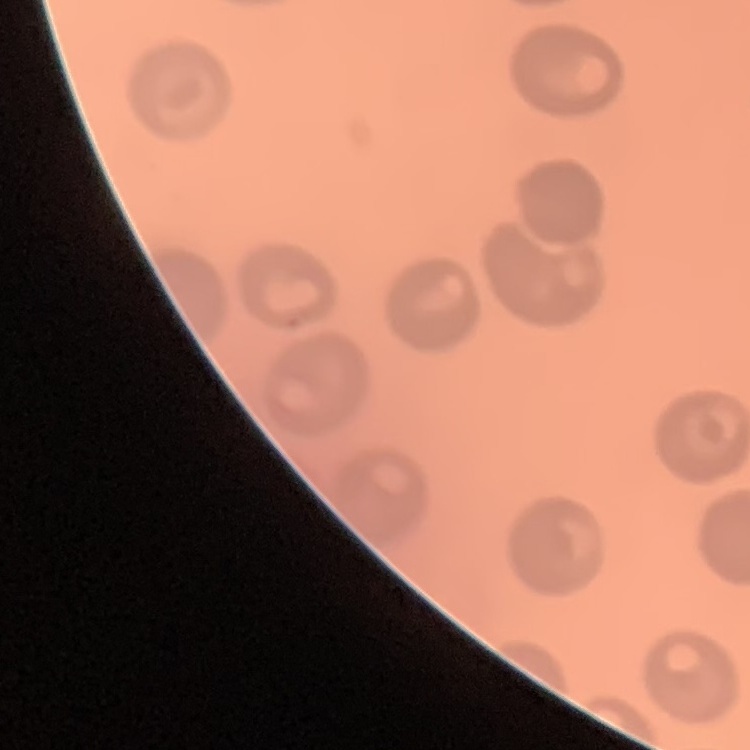

Summary:
  - Erythrocyte morphology: no rouleaux formation
  - Stain: Field's or Giemsa
  - Image type: square crop of a larger photomicrograph
  - Preparation: thin blood smear